State the blood parasite species.
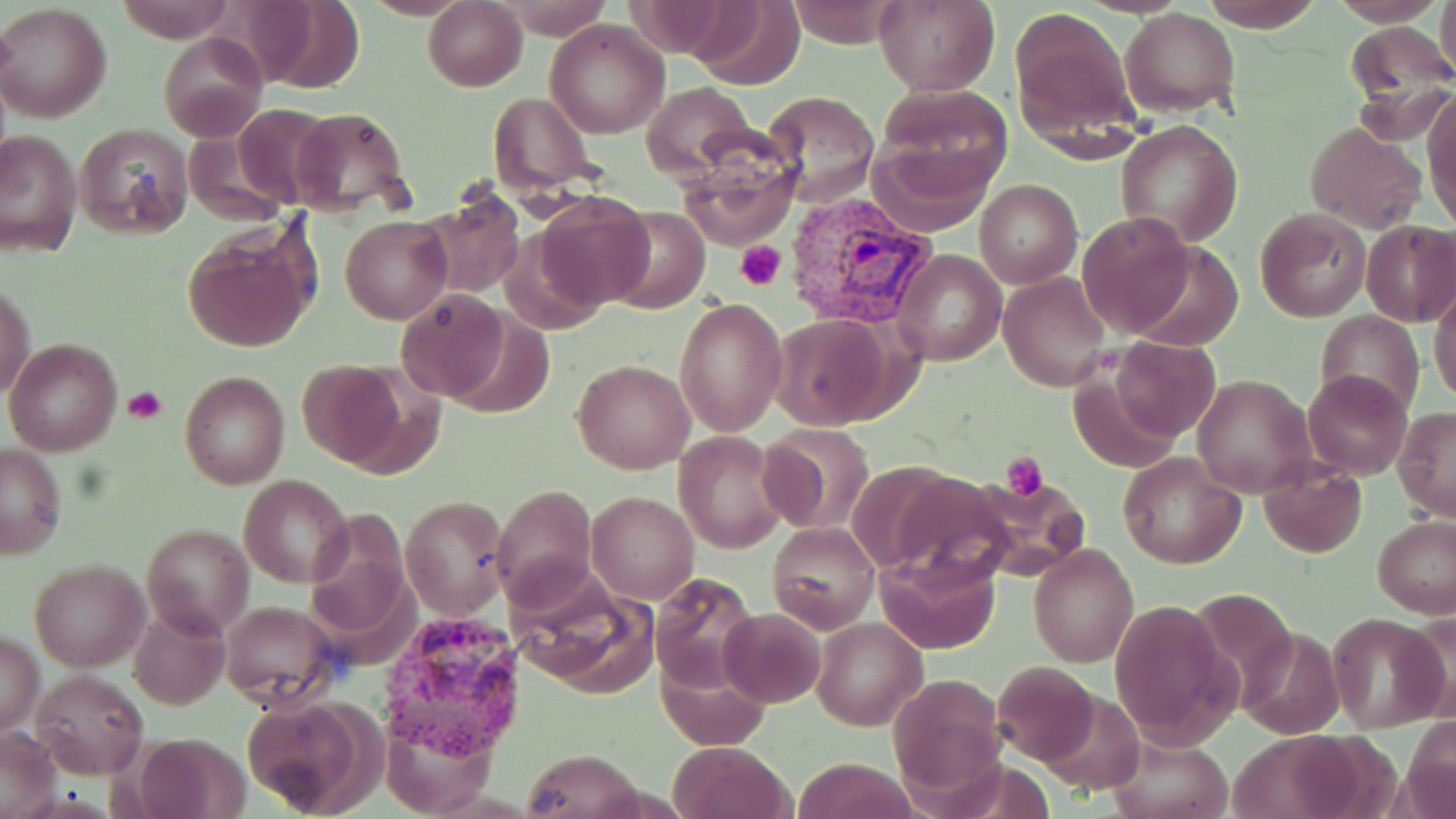
Plasmodium vivax.

Approximate bounding boxes as named x1/y1/x2/y2 corners in pixels. Platelet locations: (x1=737, y1=241, x2=786, y2=290), (x1=124, y1=386, x2=167, y2=424), (x1=1003, y1=451, x2=1049, y2=500). Plasmodium vivax-infected red blood cell locations: (x1=779, y1=190, x2=938, y2=330), (x1=380, y1=612, x2=525, y2=758). Uninfected red blood cell locations: (x1=115, y1=0, x2=234, y2=41), (x1=689, y1=0, x2=804, y2=89), (x1=783, y1=0, x2=905, y2=48), (x1=875, y1=0, x2=1000, y2=96), (x1=1199, y1=0, x2=1324, y2=32), (x1=1330, y1=0, x2=1445, y2=26), (x1=1436, y1=0, x2=1456, y2=83), (x1=424, y1=1, x2=528, y2=91), (x1=498, y1=1, x2=614, y2=36), (x1=1, y1=4, x2=112, y2=123), (x1=1010, y1=5, x2=1141, y2=142), (x1=1122, y1=9, x2=1241, y2=119), (x1=545, y1=19, x2=669, y2=138), (x1=1343, y1=23, x2=1456, y2=144), (x1=160, y1=33, x2=266, y2=141), (x1=643, y1=82, x2=754, y2=183), (x1=874, y1=83, x2=1013, y2=193), (x1=764, y1=91, x2=880, y2=206), (x1=490, y1=92, x2=602, y2=200), (x1=1423, y1=92, x2=1456, y2=230), (x1=233, y1=103, x2=336, y2=209), (x1=288, y1=107, x2=415, y2=217), (x1=1117, y1=118, x2=1243, y2=248), (x1=1305, y1=121, x2=1424, y2=234), (x1=74, y1=123, x2=193, y2=238), (x1=1, y1=129, x2=81, y2=257), (x1=869, y1=137, x2=996, y2=235), (x1=678, y1=154, x2=796, y2=249), (x1=974, y1=180, x2=1080, y2=288), (x1=419, y1=188, x2=526, y2=299), (x1=534, y1=192, x2=655, y2=310), (x1=607, y1=208, x2=710, y2=314), (x1=1255, y1=209, x2=1372, y2=322), (x1=341, y1=213, x2=453, y2=324), (x1=1077, y1=213, x2=1199, y2=337), (x1=1361, y1=219, x2=1456, y2=327), (x1=180, y1=225, x2=317, y2=353), (x1=499, y1=226, x2=608, y2=336), (x1=1125, y1=241, x2=1246, y2=349), (x1=895, y1=249, x2=1006, y2=367), (x1=999, y1=273, x2=1111, y2=393), (x1=1, y1=283, x2=35, y2=401), (x1=1430, y1=284, x2=1456, y2=407), (x1=394, y1=290, x2=509, y2=404), (x1=675, y1=296, x2=788, y2=436), (x1=1317, y1=309, x2=1423, y2=416), (x1=443, y1=311, x2=555, y2=420), (x1=771, y1=313, x2=892, y2=429), (x1=5, y1=336, x2=122, y2=456), (x1=1110, y1=338, x2=1221, y2=440), (x1=573, y1=359, x2=693, y2=473), (x1=296, y1=360, x2=412, y2=469), (x1=1301, y1=369, x2=1412, y2=479), (x1=179, y1=371, x2=290, y2=489), (x1=1069, y1=373, x2=1181, y2=475), (x1=1193, y1=374, x2=1318, y2=499), (x1=1394, y1=407, x2=1456, y2=522), (x1=760, y1=423, x2=876, y2=535), (x1=673, y1=431, x2=789, y2=554), (x1=1, y1=444, x2=68, y2=558), (x1=1119, y1=453, x2=1247, y2=568), (x1=1259, y1=455, x2=1368, y2=558), (x1=884, y1=471, x2=1021, y2=589), (x1=968, y1=474, x2=1086, y2=576), (x1=240, y1=475, x2=354, y2=588), (x1=491, y1=483, x2=598, y2=607), (x1=587, y1=492, x2=698, y2=604), (x1=401, y1=495, x2=510, y2=619), (x1=306, y1=513, x2=412, y2=646), (x1=1373, y1=514, x2=1456, y2=617), (x1=768, y1=521, x2=879, y2=631), (x1=141, y1=523, x2=253, y2=639), (x1=1028, y1=543, x2=1139, y2=666), (x1=875, y1=549, x2=1001, y2=655), (x1=30, y1=560, x2=148, y2=672), (x1=513, y1=572, x2=661, y2=696), (x1=649, y1=572, x2=762, y2=693), (x1=1108, y1=598, x2=1239, y2=751), (x1=219, y1=599, x2=339, y2=710), (x1=126, y1=606, x2=229, y2=711), (x1=720, y1=609, x2=826, y2=708), (x1=1328, y1=612, x2=1447, y2=733), (x1=812, y1=617, x2=926, y2=730), (x1=0, y1=632, x2=45, y2=739), (x1=657, y1=659, x2=771, y2=750), (x1=991, y1=662, x2=1099, y2=765), (x1=29, y1=669, x2=147, y2=778), (x1=885, y1=674, x2=1005, y2=804), (x1=1039, y1=691, x2=1148, y2=796), (x1=242, y1=696, x2=382, y2=816), (x1=383, y1=717, x2=496, y2=818), (x1=1, y1=726, x2=59, y2=816), (x1=1106, y1=732, x2=1235, y2=819), (x1=1229, y1=732, x2=1364, y2=818), (x1=131, y1=733, x2=253, y2=819), (x1=669, y1=741, x2=791, y2=819), (x1=520, y1=749, x2=642, y2=819), (x1=790, y1=757, x2=920, y2=819). Single field of view. Optical microscopy. May-Grünwald-Giemsa-stained preparation. Captured at 1000x magnification. Image is 1456×819 pixels. Thin blood smear.